Classify this cell by malaria status.
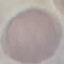
It is uninfected.

{
  "capture": "smartphone through the microscope eyepiece",
  "image_type": "automatically extracted cell patch, resized to 64 × 64 pixels",
  "preparation": "thin blood smear",
  "stain": "Giemsa"
}